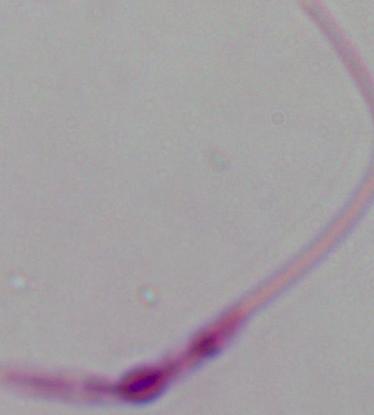

identification = Leishmania
magnification = 1000x
modality = micrograph